Report the malaria status of this cell.
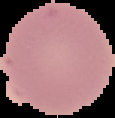
Uninfected.

{
  "image_size": "115×118 pixels",
  "preparation": "thin blood film",
  "image_type": "segmented cell region on a black background"
}